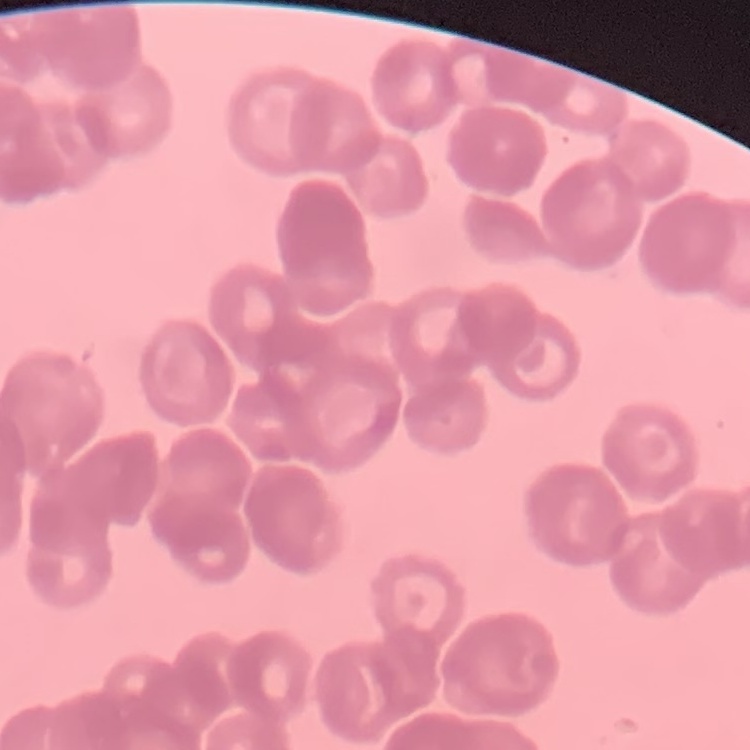

The red blood cells show rouleaux formation. Stained with either Field's or Giemsa. Thin peripheral smear. Square crop of a larger photomicrograph.